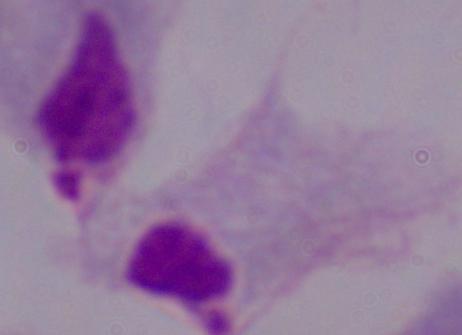
modality: photomicrograph
magnification: 1000x
identification: trichomonad